Assess the morphology of the red blood cells.
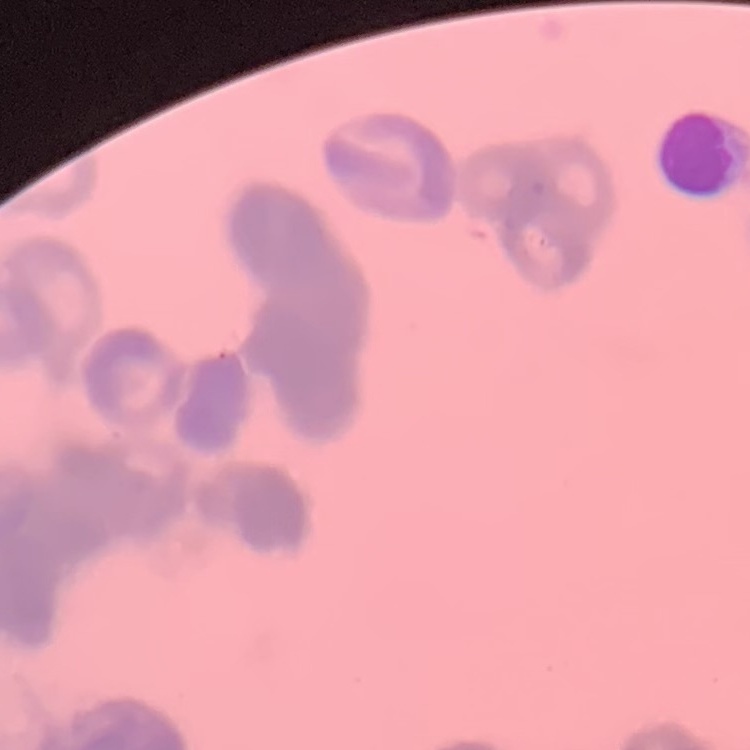

Rouleaux formation.

Field's or Giemsa stain. Thin peripheral smear. One tile cut from a larger photomicrograph.